Identify the parasite.
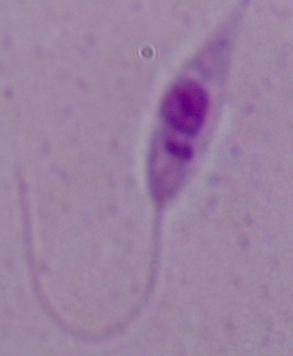
Leishmania.

magnification: 1000x
modality: photomicrograph